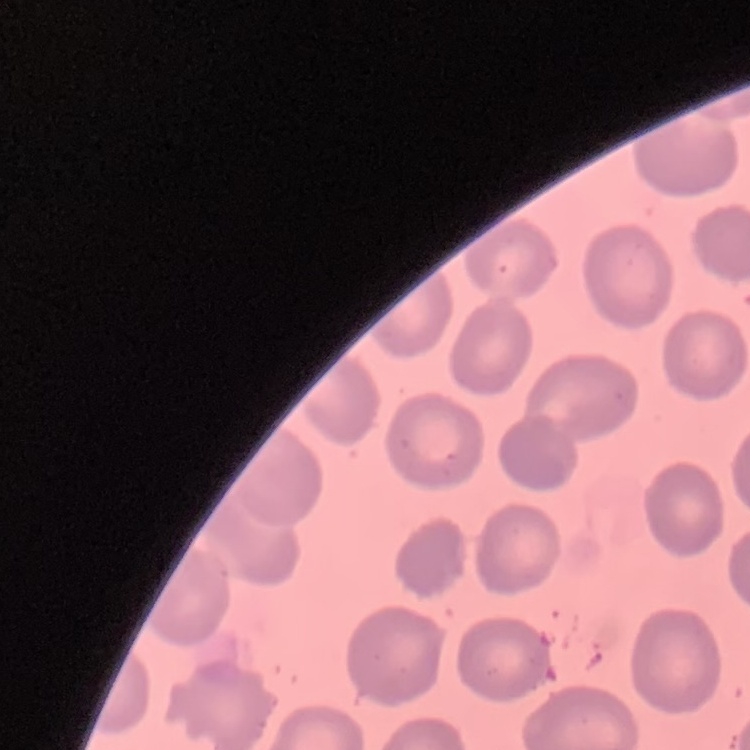

Summary:
  - Erythrocyte morphology: no rouleaux formation
  - Preparation: thin peripheral smear
  - Image type: one tile cut from a larger photomicrograph
  - Stain: Field's or Giemsa